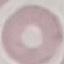
Summary:
  - Malaria status: uninfected
  - Stain: Giemsa
  - Image type: automatically extracted cell patch, resized to 64 × 64 pixels
  - Capture: smartphone camera at the microscope eyepiece
  - Preparation: thin smear